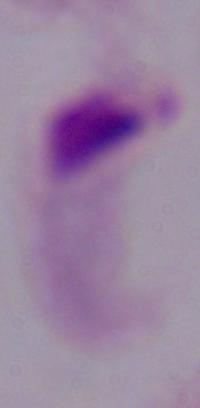
Summary:
  - Modality: micrograph
  - Identification: trichomonad
  - Magnification: 1000x